Name the blood parasite species.
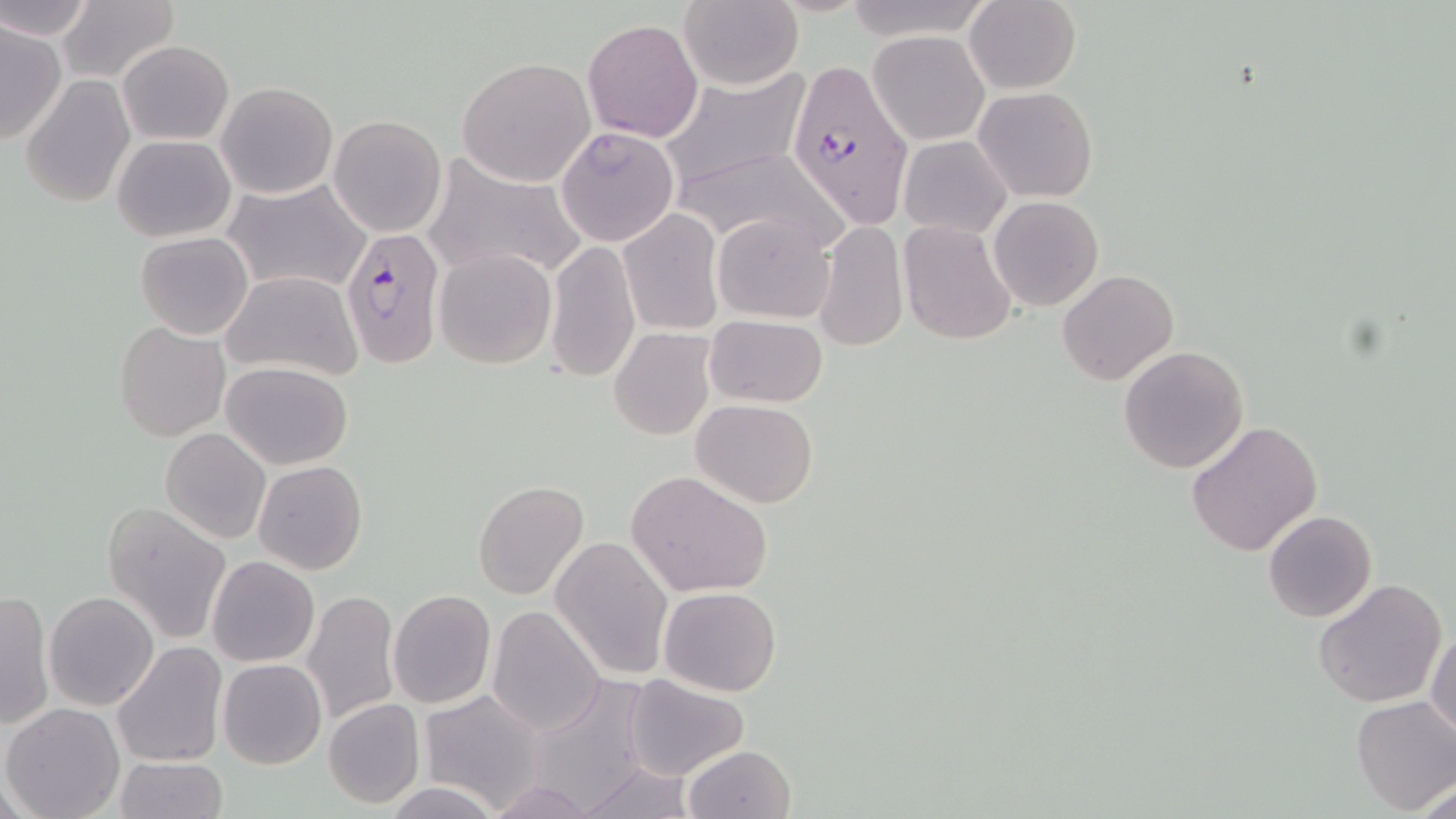

Plasmodium falciparum.

field of view = one of a larger specimen
preparation = thin blood smear
modality = optical microscopy
stain = May-Grünwald-Giemsa
image size = 1456×819 pixels
magnification = 1000x
uninfected red blood cell locations = approximate bounding boxes as [x1, y1, x2, y2] in pixels: [0, 0, 93, 41], [678, 0, 801, 91], [965, 0, 1081, 94], [57, 2, 178, 84], [583, 18, 703, 142], [0, 19, 67, 144], [869, 31, 989, 145], [119, 40, 233, 144], [457, 56, 594, 185], [661, 67, 813, 195], [21, 73, 135, 209], [216, 81, 338, 199], [974, 86, 1096, 203], [329, 115, 446, 237], [555, 125, 678, 247], [113, 134, 236, 241], [899, 135, 1011, 239], [676, 148, 840, 254], [423, 155, 589, 281], [223, 177, 373, 296], [988, 195, 1103, 311], [616, 208, 724, 335], [711, 211, 837, 323], [814, 219, 909, 352], [899, 220, 1016, 343], [135, 232, 253, 340], [545, 240, 640, 383], [434, 247, 557, 368], [1056, 269, 1179, 385], [221, 270, 362, 382], [704, 315, 829, 407], [115, 322, 229, 440], [609, 328, 715, 440], [1118, 346, 1249, 473], [221, 360, 354, 469], [691, 399, 819, 508], [1187, 420, 1323, 557], [159, 427, 270, 545], [252, 460, 368, 575], [625, 470, 772, 598], [471, 480, 590, 600], [104, 503, 230, 644], [1262, 509, 1377, 623], [1287, 529, 1414, 666], [550, 535, 673, 680], [207, 557, 319, 667], [1313, 578, 1448, 707], [659, 586, 782, 695], [1, 589, 54, 731], [303, 589, 400, 726], [388, 590, 495, 709], [45, 592, 159, 710], [487, 604, 605, 736], [1427, 625, 1456, 744], [112, 641, 228, 769], [216, 659, 327, 770], [622, 675, 750, 781], [419, 689, 546, 811], [1351, 696, 1456, 814], [323, 697, 425, 808], [3, 703, 126, 818], [682, 744, 797, 819], [115, 757, 227, 818], [574, 762, 699, 819], [1417, 777, 1455, 819], [484, 779, 598, 817], [382, 782, 504, 819]
Plasmodium falciparum-infected red blood cell locations = approximate bounding boxes as [x1, y1, x2, y2] in pixels: [785, 61, 915, 227], [340, 226, 445, 369]